Name the parasite shown.
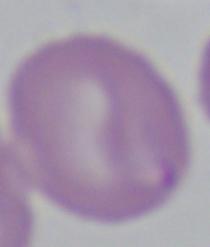

Babesia.

Captured at 1000x magnification. Photomicrograph.